State the blood parasite species.
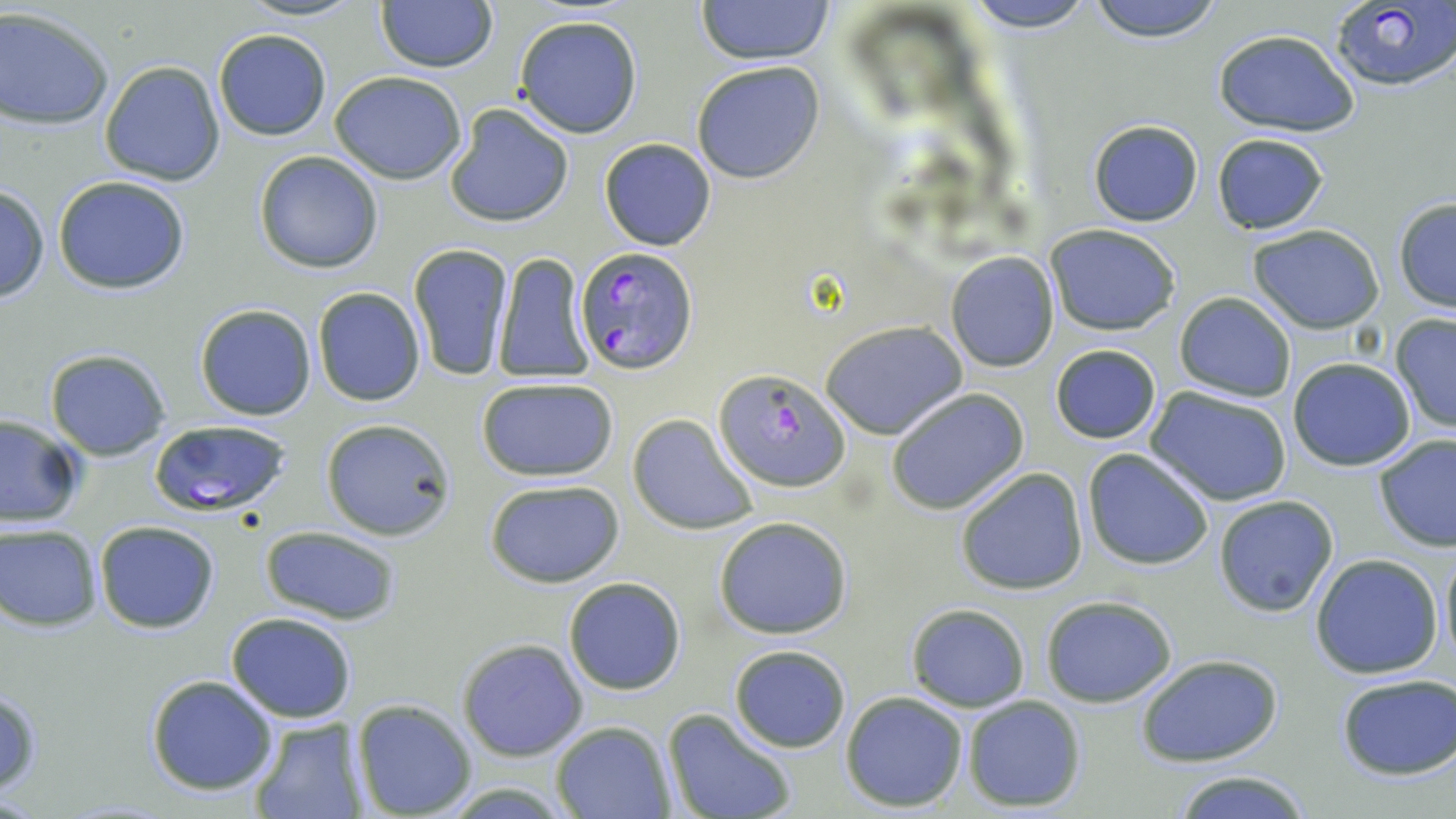
Plasmodium falciparum.

Summary:
  - Coordinate format: approximate bounding boxes as [x1, y1, x2, y2] in pixels
  - Uninfected red blood cell locations: [238, 0, 364, 22], [695, 0, 836, 63], [962, 0, 1097, 33], [1085, 0, 1227, 42], [376, 1, 496, 72], [0, 8, 113, 129], [513, 15, 643, 138], [212, 28, 331, 139], [1212, 29, 1359, 136], [100, 59, 225, 186], [690, 61, 825, 184], [330, 70, 469, 183], [444, 102, 575, 228], [1089, 119, 1203, 227], [1211, 133, 1328, 236], [599, 137, 717, 251], [254, 150, 384, 274], [53, 176, 192, 295], [0, 183, 49, 303], [1393, 199, 1456, 313], [1045, 223, 1181, 336], [1248, 224, 1387, 332], [408, 242, 512, 381], [492, 250, 594, 383], [945, 252, 1060, 373], [313, 286, 426, 407], [1173, 292, 1297, 402], [195, 304, 317, 421], [1390, 313, 1456, 434], [821, 320, 967, 438], [1050, 345, 1161, 444], [44, 348, 173, 460], [1287, 357, 1417, 471], [476, 377, 619, 482], [1146, 386, 1294, 505], [885, 387, 1030, 515], [629, 413, 757, 536], [0, 414, 85, 529], [320, 419, 457, 541], [1373, 434, 1456, 552], [1082, 448, 1216, 570], [955, 466, 1089, 596], [483, 479, 628, 586], [1212, 494, 1339, 617], [714, 516, 853, 639], [94, 521, 221, 633], [1, 524, 103, 630], [260, 525, 401, 626], [1438, 543, 1455, 670], [1309, 553, 1445, 679], [562, 575, 688, 695], [1041, 597, 1177, 708], [905, 603, 1030, 711], [226, 611, 357, 724], [457, 638, 587, 761], [729, 644, 851, 752], [1136, 653, 1284, 767], [1335, 673, 1456, 782], [144, 674, 280, 795], [0, 689, 43, 796], [840, 691, 968, 812], [960, 695, 1087, 812], [350, 698, 478, 819], [662, 708, 797, 819], [246, 717, 360, 819], [550, 721, 675, 819], [1169, 769, 1314, 819]
  - Plasmodium falciparum-infected red blood cell locations: [1331, 0, 1456, 91], [576, 246, 701, 375], [713, 367, 850, 491], [148, 418, 294, 518]
  - Image size: 1456×819 pixels
  - Stain: May-Grünwald-Giemsa
  - Modality: optical microscopy
  - Preparation: thin blood film
  - Field of view: one of a larger specimen
  - Magnification: 1000x